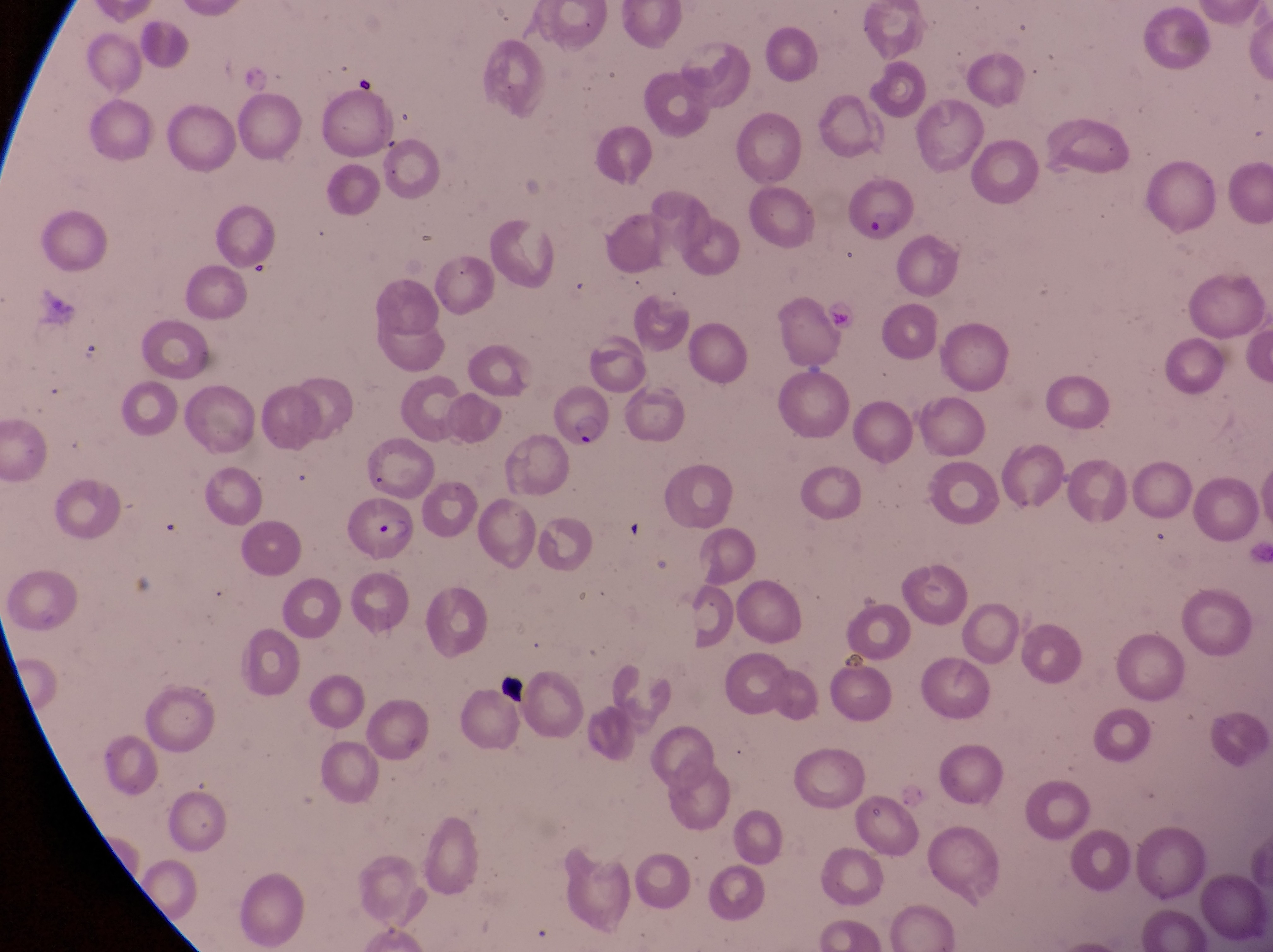

Approximate bounding boxes as {left, top, right, bottom} in pixels. Artifact (platelet-like body, stain precipitate, or debris) locations: {497, 669, 532, 706}. Parasitised red blood cell locations: {847, 183, 916, 243}, {547, 382, 621, 452}, {349, 499, 421, 569}. Image is 1273×952 pixels. Captured by a smartphone held over the eyepiece of an Olympus CX-23 microscope. Magnification of 1000x. Collected in Uganda. One field of view. Thin blood film.